Identify the cell.
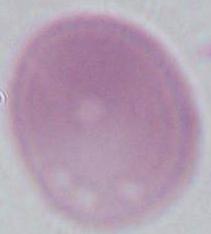
An erythrocyte.

Summary:
  - Modality: photomicrograph
  - Magnification: 1000x